Report the malaria status of this cell.
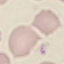

Uninfected.

capture = smartphone through the microscope eyepiece
preparation = thin blood film
stain = Giemsa
image type = automatically extracted cell patch, resized to 64 × 64 pixels